Classify this cell by malaria status.
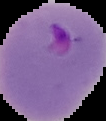

Parasitized.

Summary:
  - Preparation: thin blood film
  - Image size: 106×121 pixels
  - Image type: cell region segmented out of the field of view; surrounding area masked to black